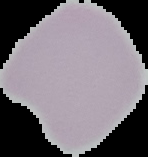
preparation: thin blood film
malaria_status: uninfected
image_size: 148×157 pixels
image_type: cell region segmented out of the field of view; surrounding area masked to black